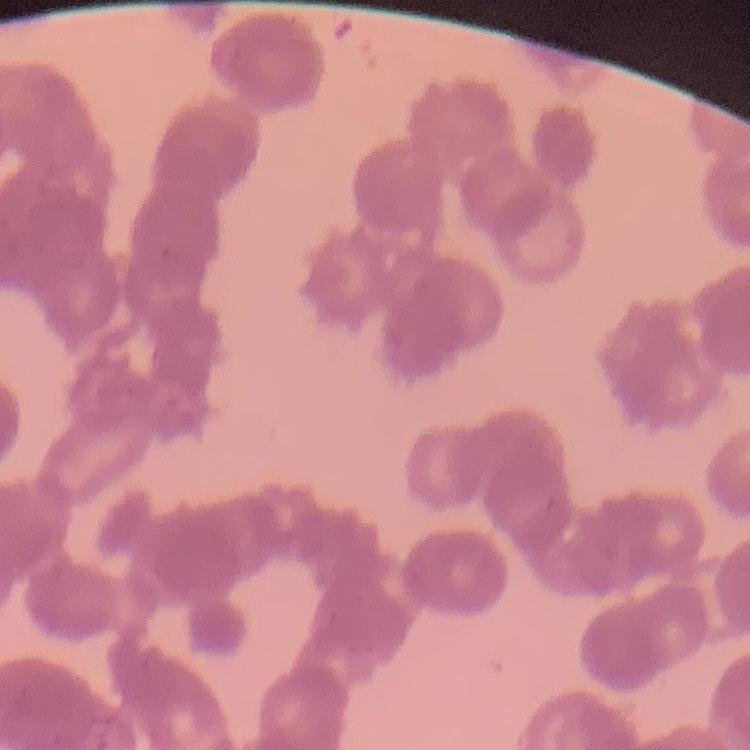
Summary:
  - Erythrocyte morphology: rouleaux formation
  - Preparation: thin blood film
  - Image type: one tile cut from a larger photomicrograph
  - Stain: Field's or Giemsa